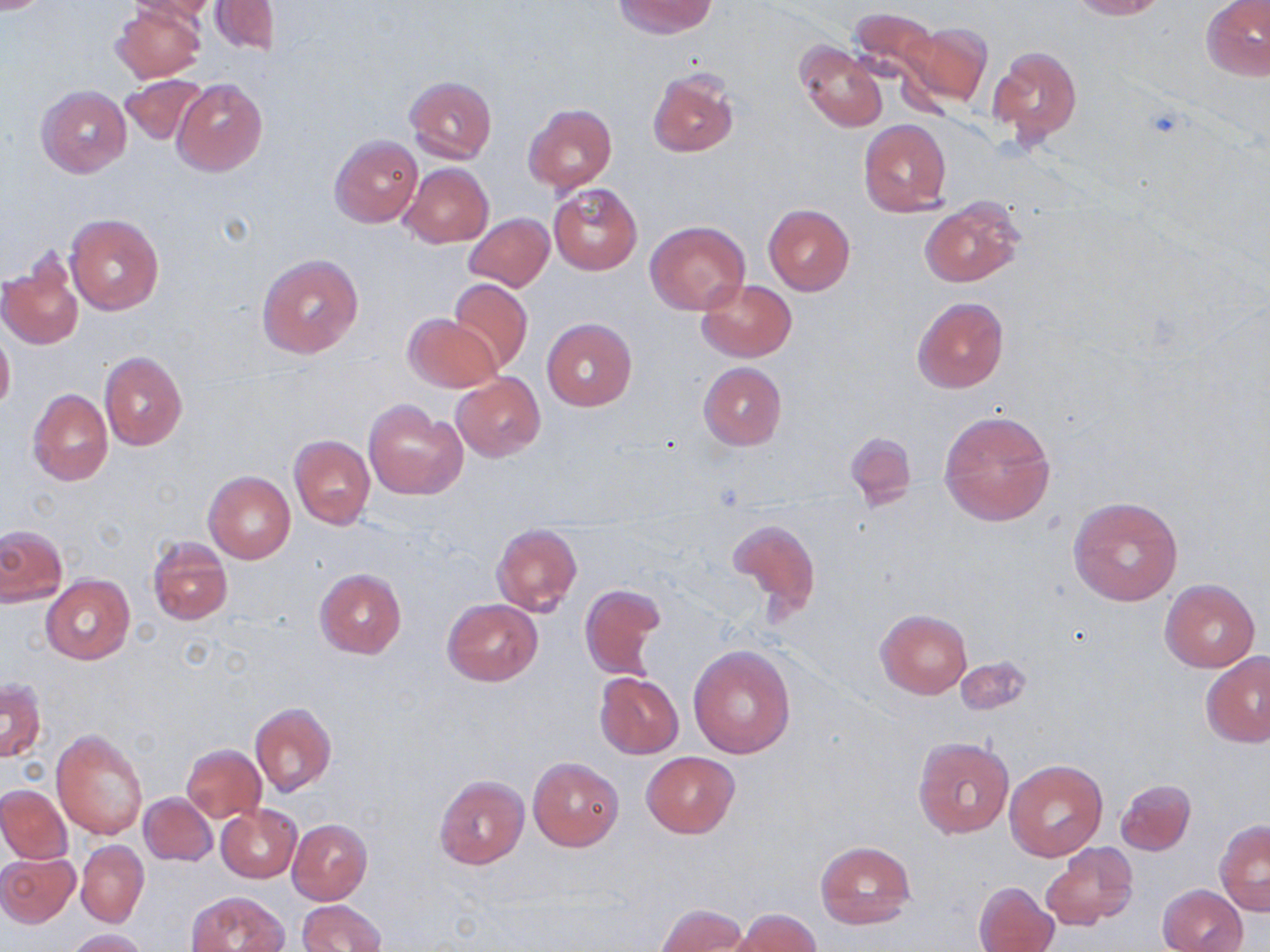
slide_level_diagnosis: no evidence of blood parasites
preparation: thin blood film
uninfected_red_blood_cell_locations: 'approximate bounding boxes as (x1,y1)-(x2,y2) corner pairs in pixels: (0,0)-(56,13), (127,0)-(218,23), (614,0)-(716,38), (1069,0)-(1166,19), (1202,0)-(1269,81), (212,1)-(280,54), (113,3)-(206,83), (846,9)-(948,103), (897,20)-(992,109), (795,41)-(887,132), (989,46)-(1083,146), (648,69)-(738,157), (119,74)-(209,145), (404,76)-(497,163), (172,80)-(267,175), (36,84)-(131,178), (522,104)-(616,193), (858,119)-(953,217), (329,135)-(422,227), (399,162)-(493,247), (547,181)-(643,275), (919,199)-(1024,286), (763,204)-(856,295), (66,213)-(164,316), (464,213)-(554,292), (645,220)-(750,314), (259,254)-(363,358), (1,259)-(83,350), (448,278)-(534,372), (697,279)-(796,361), (912,296)-(1009,392), (403,313)-(500,392), (542,318)-(636,410), (0,329)-(15,414), (99,352)-(187,451), (698,362)-(786,450), (451,374)-(545,460), (28,389)-(112,486), (364,399)-(466,499), (939,409)-(1056,526), (847,432)-(915,505), (289,434)-(374,530), (204,471)-(295,564), (1069,495)-(1182,606), (725,516)-(822,625), (492,524)-(581,615), (0,526)-(66,606), (146,537)-(233,626), (315,568)-(406,658), (42,575)-(135,664), (1160,579)-(1260,671), (581,584)-(664,680), (442,598)-(542,686), (876,609)-(972,698), (687,645)-(796,759), (1202,652)-(1270,748), (952,659)-(1032,714), (595,672)-(683,758), (1,679)-(45,763), (248,703)-(336,797), (53,729)-(148,840), (913,736)-(1013,837), (182,744)-(266,822), (641,752)-(740,838), (528,756)-(624,851), (1003,759)-(1107,862), (434,775)-(528,868), (1115,778)-(1196,856), (0,785)-(72,864), (139,792)-(217,866), (216,805)-(300,882), (288,819)-(372,904), (1215,820)-(1270,914), (76,840)-(148,927), (814,840)-(916,931), (1040,844)-(1138,928), (0,852)-(79,927), (974,880)-(1061,952), (1157,883)-(1248,951), (188,891)-(288,952), (297,900)-(386,952), (656,903)-(750,952), (729,909)-(821,952), (65,928)-(148,951)'
stain: May-Grünwald-Giemsa
magnification: 1000x
image_size: 1270×952 pixels
field_of_view: one of a larger specimen
modality: optical microscopy